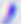

identification: Toxoplasma gondii
magnification: 400x
modality: photomicrograph